State which parasite is depicted.
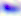

This is Toxoplasma gondii.

Micrograph. Captured at 400x magnification.